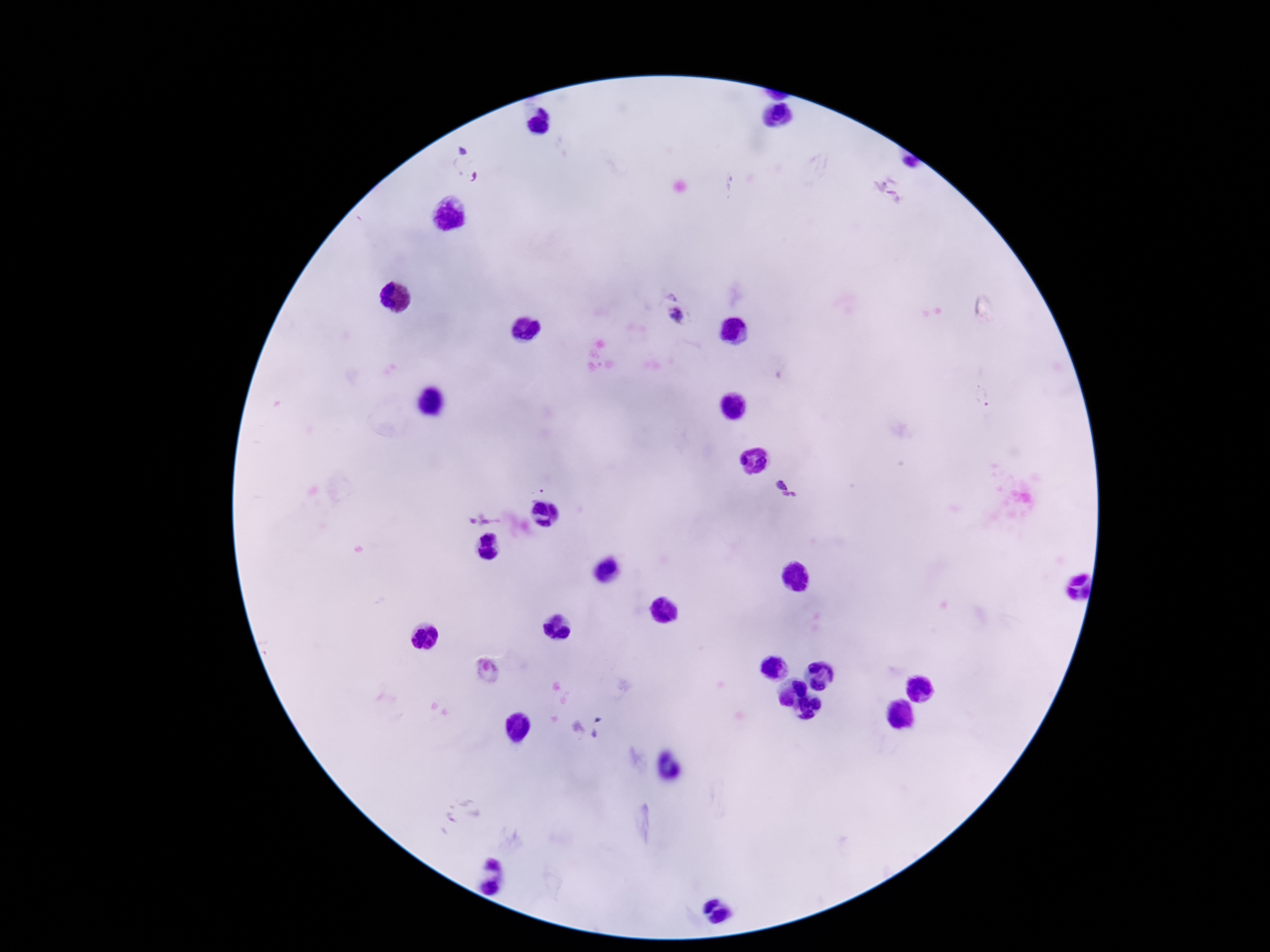

Approximate centers as {x, y} in pixels.
Summary:
  - Plasmodium parasite locations: {467, 164}, {889, 190}, {678, 318}, {982, 397}, {786, 488}, {538, 489}, {483, 516}, {489, 669}
  - Patient malaria status: positive
  - Capture: smartphone camera through the microscope eyepiece
  - Field of view: one from this slide
  - Magnification: 100x
  - Preparation: thick blood film
  - Image size: 1270×952 pixels
  - Stain: Giemsa